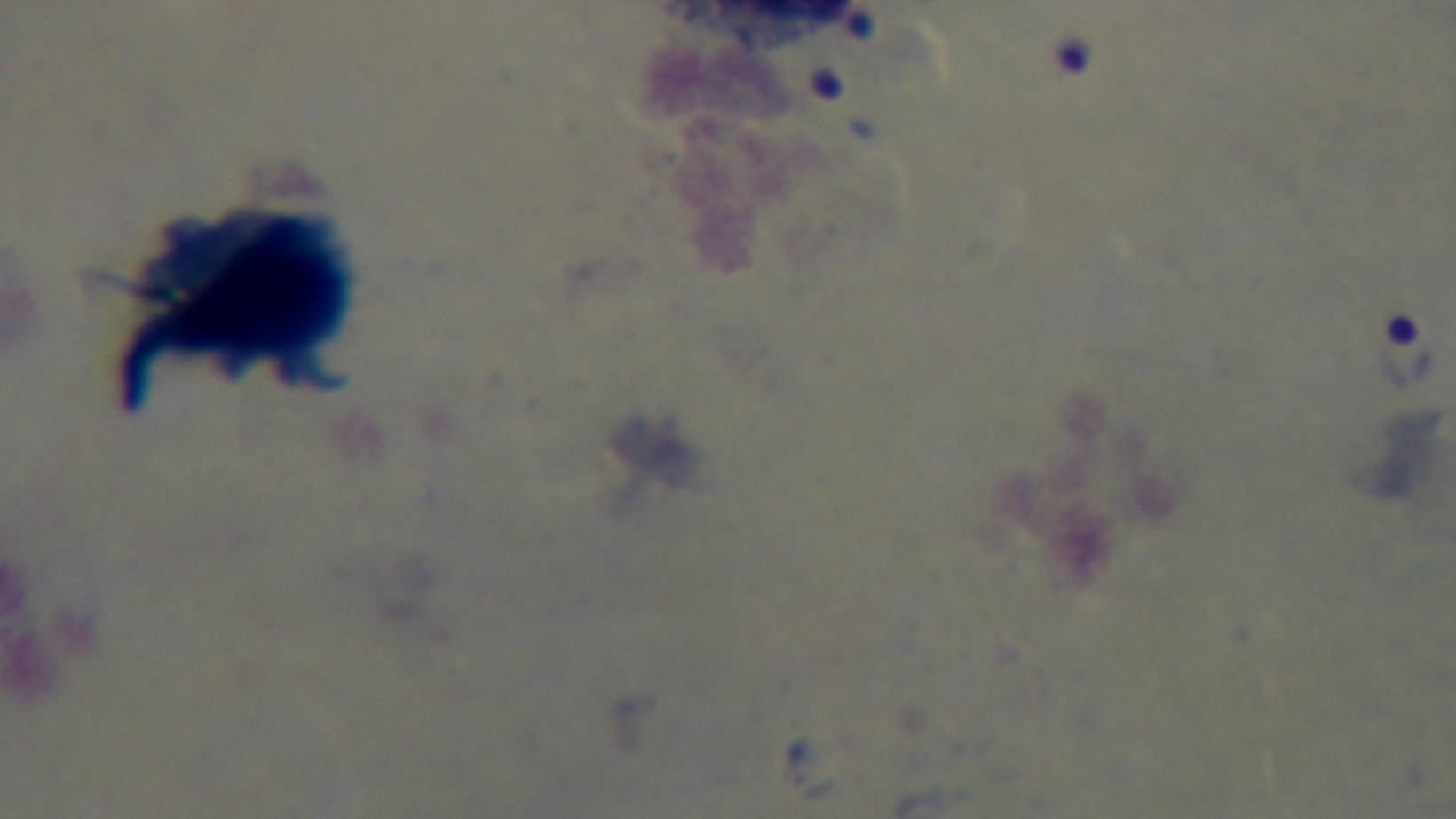
Summary:
  - Objective: 100x oil immersion
  - Capture: mounted 4K digital camera
  - Malaria status: positive
  - Field of view: single
  - Stain: Giemsa
  - Preparation: thick smear
  - Modality: light microscopy